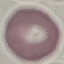

{
  "result": "no malaria parasites seen",
  "capture": "smartphone through the microscope eyepiece",
  "image_type": "automatically extracted cell patch, resized to 64 × 64 pixels",
  "preparation": "thin blood smear",
  "stain": "Giemsa"
}